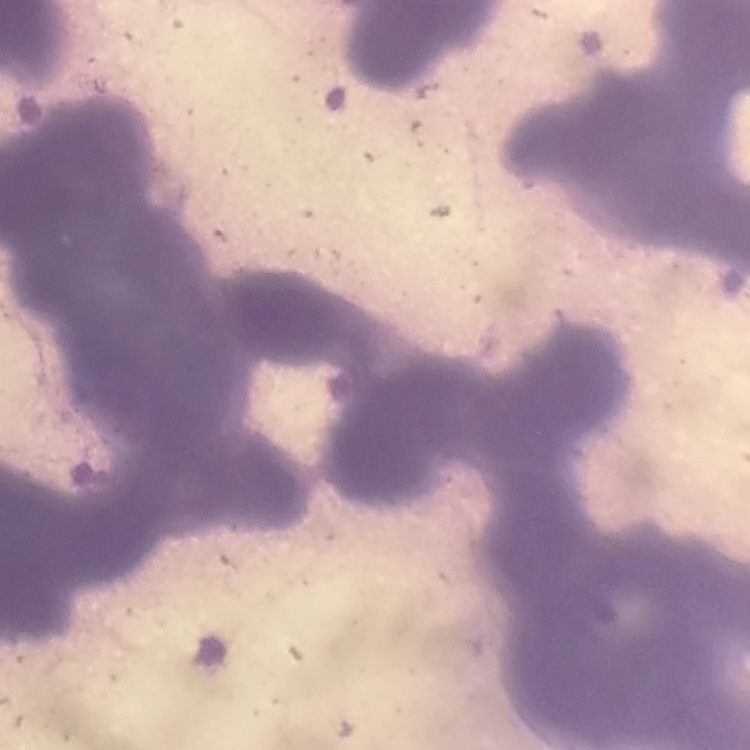

Summary:
  - Red blood cell morphology: rouleaux formation
  - Image type: one tile cut from a larger photomicrograph
  - Stain: Field's or Giemsa
  - Preparation: thin blood film